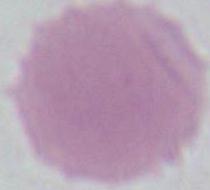

identification = erythrocyte
magnification = 1000x
modality = micrograph